Assess for Plasmodium parasites.
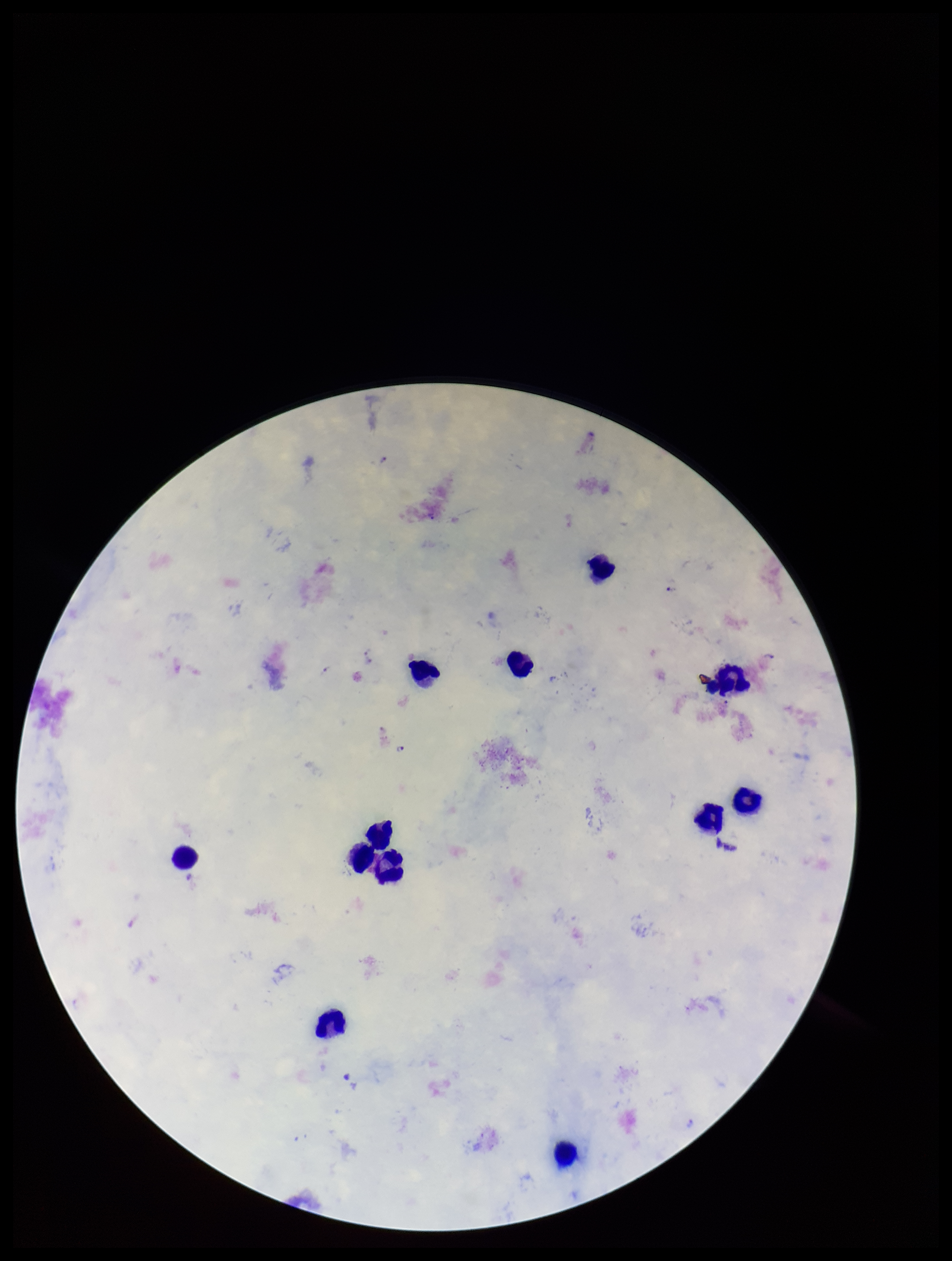

Detected.

Giemsa stain. Leukocyte count: 12. Parasite count: 3. Single field of view. Species reported for this patient: Plasmodium falciparum. Patient malaria status: infected. Image is 952×1261 pixels. Smartphone photograph taken through the eyepiece of a microscope. Preparation: thick smear.